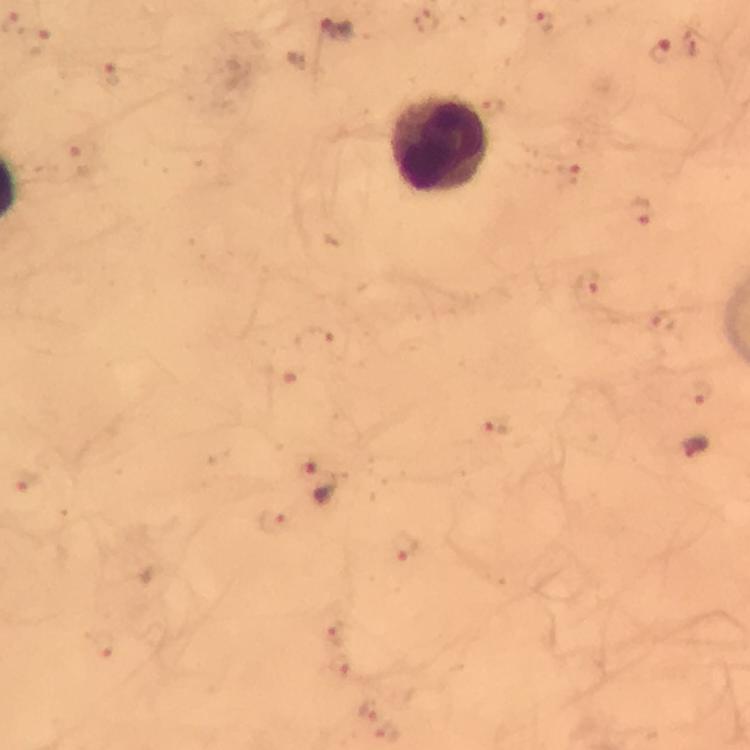

Approximate centers as {x, y} in pixels. Leukocyte locations: {438, 144}. Plasmodium parasite locations: {543, 20}, {336, 29}, {38, 41}, {660, 53}, {112, 76}, {82, 158}, {569, 173}, {642, 211}, {589, 290}, {665, 322}, {312, 342}, {699, 394}, {498, 425}, {694, 446}, {24, 480}, {316, 482}, {272, 521}, {406, 547}, {336, 632}, {101, 644}, {340, 667}, {369, 708}, {386, 734}. Giemsa-stained preparation. Immersion oil applied. At 100x magnification. Thick blood smear. Image is 750×750 pixels. From a diagnostic examination for malaria. A crop from one field of view. Photographed through the microscope with a smartphone camera.